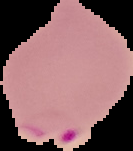

Summary:
  - Image size: 133×151 pixels
  - Preparation: thin blood smear
  - Image type: segmented cell region with the area outside set to black
  - Malaria status: parasitized